Classify this cell by malaria status.
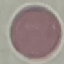

It is uninfected.

stain: Giemsa
image_type: cell patch, automatically extracted from a larger field of view and resized to 64 × 64 pixels
capture: smartphone through the microscope eyepiece
preparation: thin blood smear